Assess the morphology of the red blood cells.
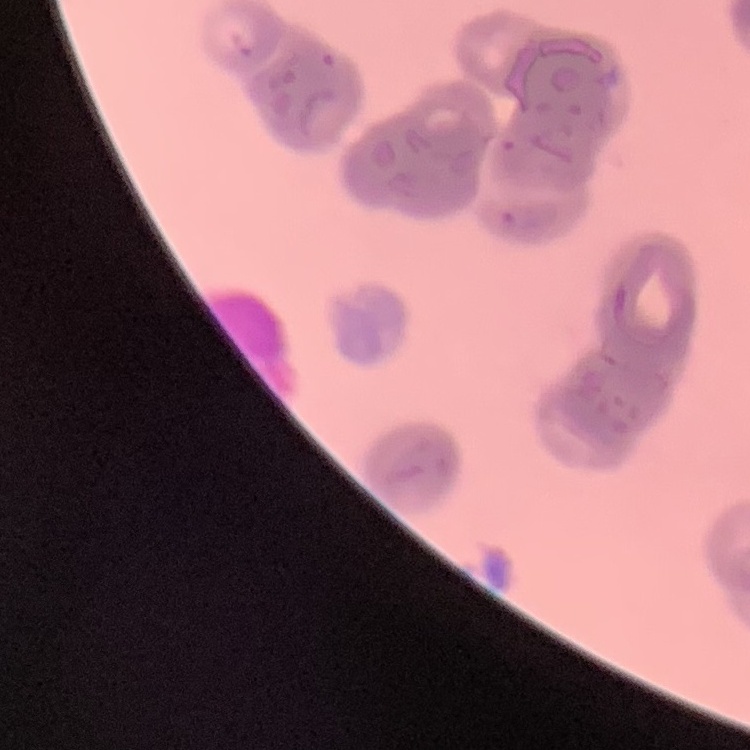

They show rouleaux formation.

image type = square crop of a larger photomicrograph
preparation = thin blood smear
stain = Field's or Giemsa